Report the malaria status of this cell.
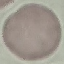

It is uninfected.

Acquired by smartphone through the microscope eyepiece. Cell patch, automatically extracted from a larger field of view and resized to 64 × 64 pixels. Giemsa stain. Thin smear of blood.